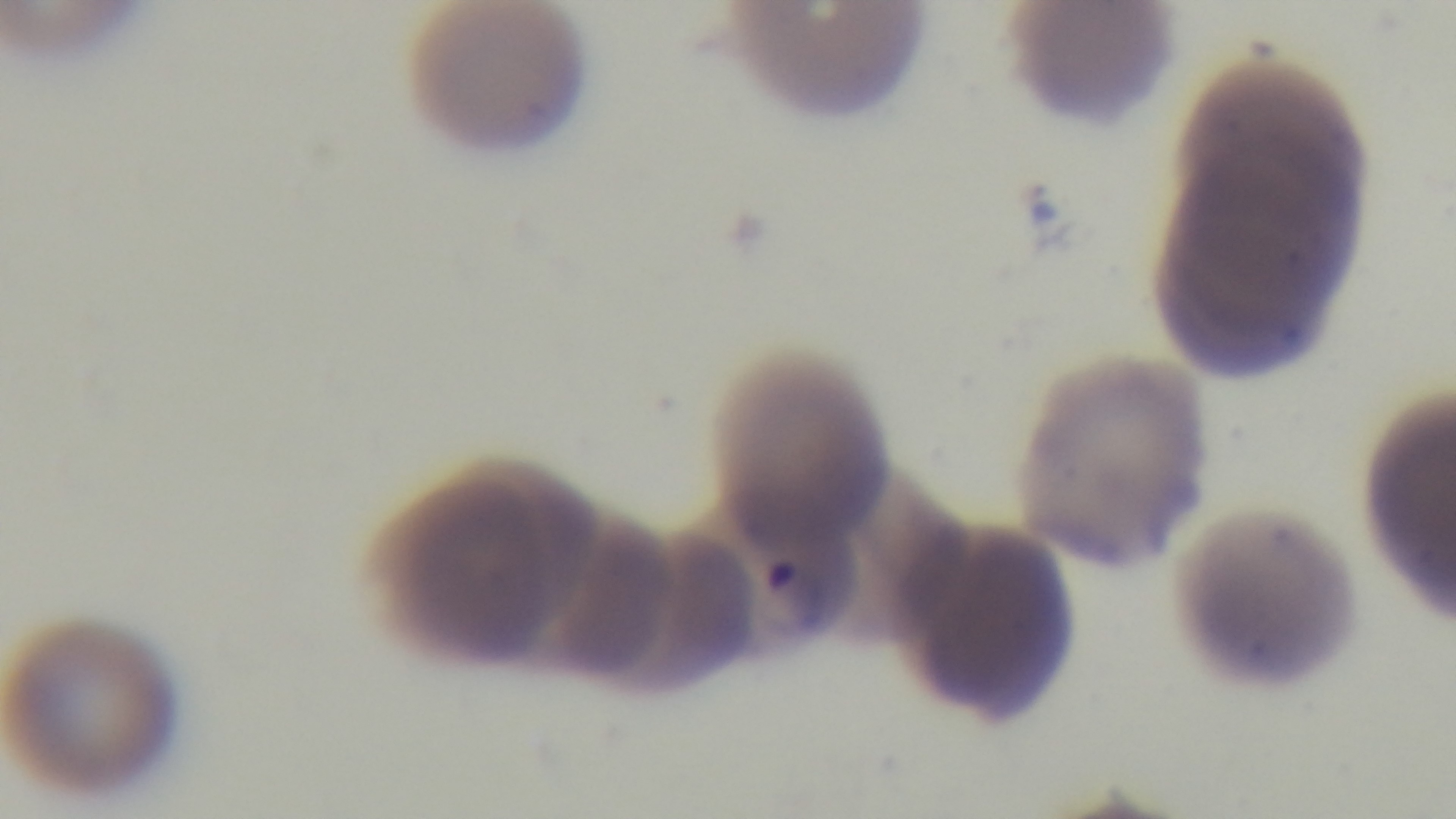
{
  "capture": "mounted 4K digital camera",
  "field_of_view": "one from the slide",
  "malaria_status": "infected",
  "objective": "100x oil immersion",
  "preparation": "thin blood film",
  "stain": "Giemsa",
  "modality": "light microscopy"
}